Give the position of every Plasmodium parasite.
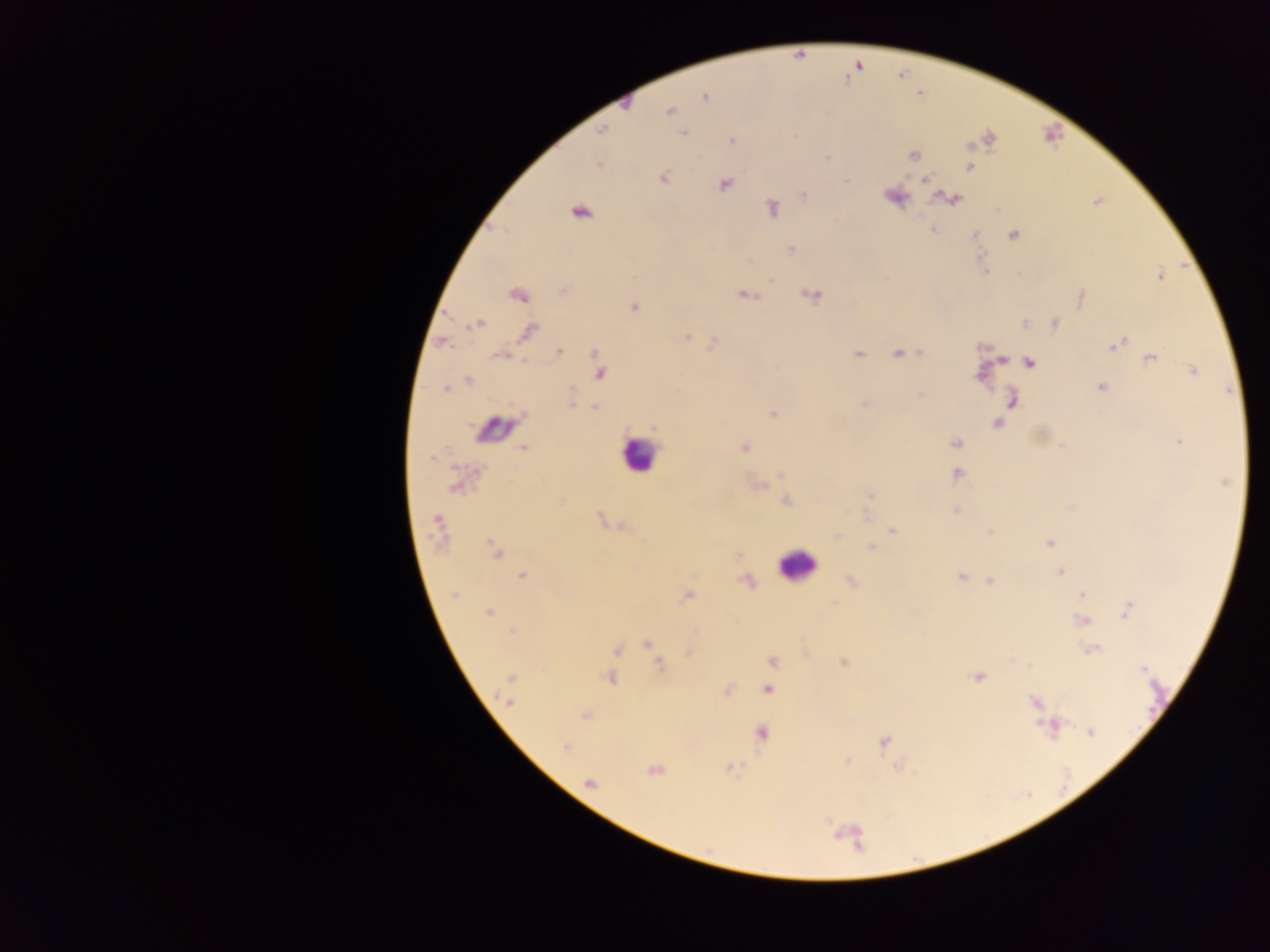
Approximate centers as (x, y) in pixels.
Plasmodium parasites: (705, 95), (626, 102), (669, 110), (601, 131), (683, 132), (988, 138), (731, 140), (913, 154), (827, 157), (598, 164), (969, 166), (662, 177), (925, 179), (846, 180), (724, 183), (804, 195), (892, 195), (954, 197), (1098, 200), (771, 209), (580, 210), (933, 229), (1012, 234), (974, 235), (790, 250), (985, 272), (1160, 275), (770, 280), (564, 289), (517, 294), (810, 294), (744, 295), (1080, 298), (633, 306), (477, 323), (1025, 323), (1054, 323), (528, 332), (686, 337), (441, 341), (713, 343), (1116, 344), (918, 351), (559, 352), (595, 353), (858, 353), (898, 353), (503, 355), (1149, 358), (1029, 362), (1194, 369), (599, 372), (468, 380), (1100, 386), (446, 388), (920, 393), (1011, 400), (572, 402), (864, 405), (594, 407), (773, 413), (996, 422), (654, 427), (1179, 441), (955, 444), (743, 447), (523, 448), (781, 474), (957, 474), (457, 484), (759, 486), (869, 495), (786, 501), (561, 502), (1071, 507), (956, 510), (600, 519), (621, 526), (438, 529), (892, 530), (989, 532), (836, 535), (1049, 542), (871, 547), (495, 553), (1059, 571), (521, 575), (962, 576), (850, 580), (989, 581), (746, 582), (454, 594), (1081, 595), (686, 596), (833, 603), (1127, 609), (487, 612), (1082, 621), (511, 631), (646, 644), (616, 649), (1091, 650), (688, 653), (805, 654), (772, 661), (844, 661), (660, 666), (1143, 669), (610, 677), (978, 677), (510, 679), (767, 689), (509, 690), (727, 690), (508, 701), (1034, 703), (585, 715), (1049, 726), (1090, 732), (761, 734), (883, 741), (565, 747), (846, 761), (728, 768), (654, 770), (589, 782).

capture = mobile-phone photograph through a microscope
preparation = thick blood film
leukocyte locations = approximate centers as (x, y) in pixels: (493, 431), (638, 454), (796, 565)
country = Ghana
field of view = single
image size = 1270×952 pixels